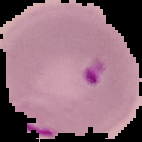
The area outside the segmented cell region is set to black. From a thin blood film. Malaria status: parasitized. Image is 142×142 pixels.